Describe the morphology of the erythrocytes.
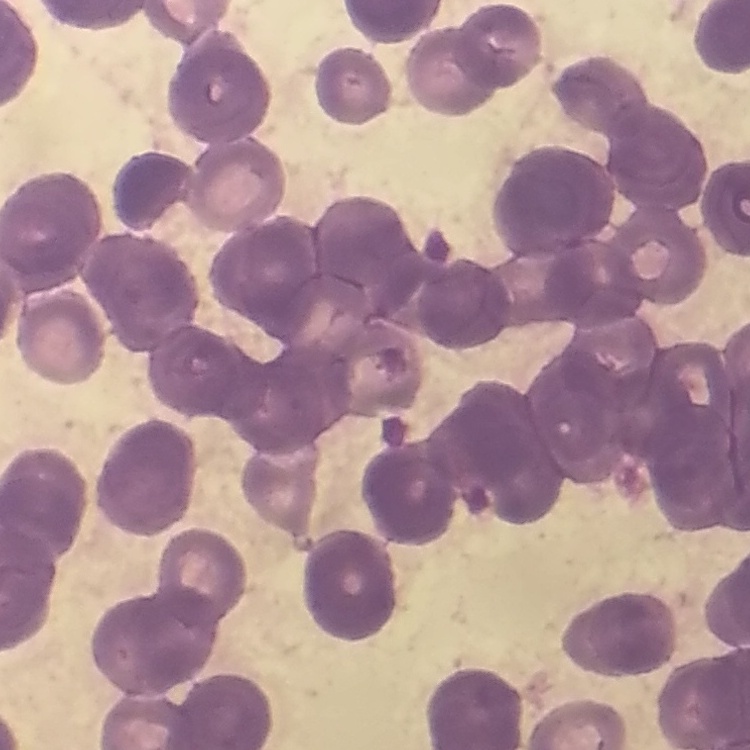

They show rouleaux formation.

Thin blood film. Field's or Giemsa stain. One tile cut from a larger photomicrograph.